Comment on the morphology of the red blood cells.
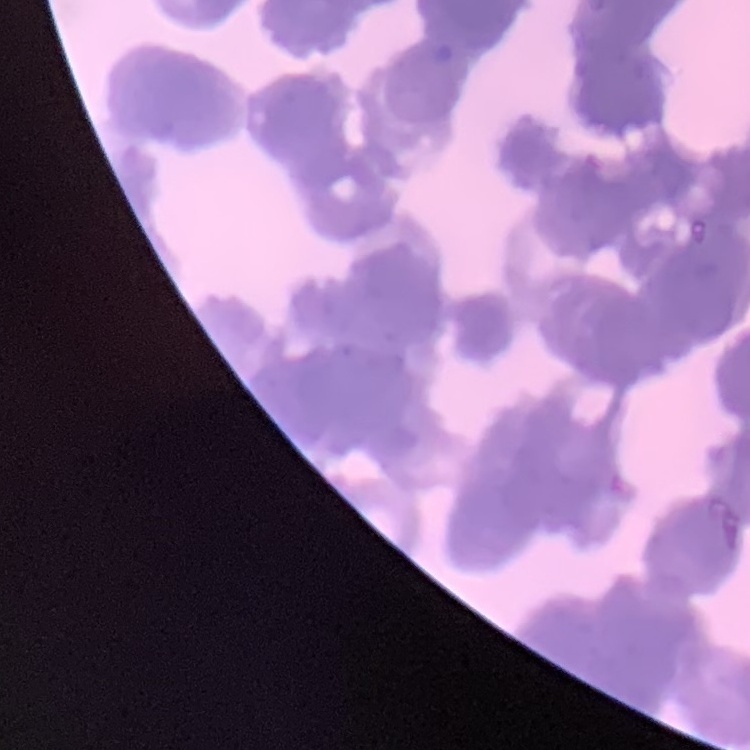

They show rouleaux formation.

{
  "preparation": "thin blood smear",
  "image_type": "square crop of a larger photomicrograph",
  "stain": "Field's or Giemsa"
}